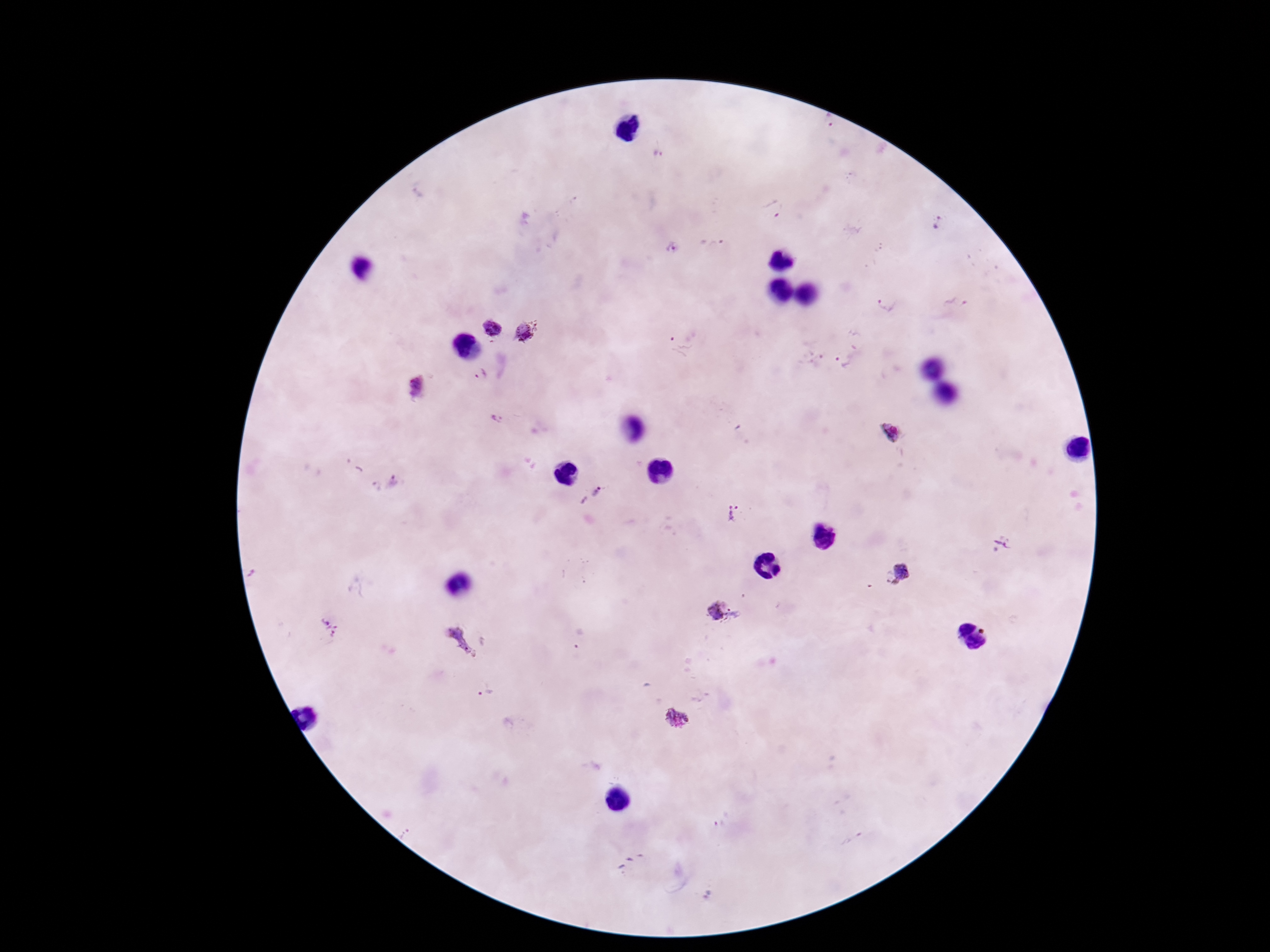
stain = Giemsa
patient malaria status = positive
preparation = thick blood smear
Plasmodium parasite locations = approximate centers as [x, y] in pixels: [828, 122], [656, 154], [775, 209], [937, 223], [674, 248], [954, 297], [888, 304], [492, 327], [526, 332], [677, 348], [843, 364], [479, 374], [415, 390], [496, 420], [889, 433], [395, 483], [374, 486], [592, 495], [732, 513], [1000, 544], [895, 575], [723, 614], [331, 631], [461, 641], [485, 692], [677, 718]
field of view = single
image size = 1270×952 pixels
capture = smartphone camera through the microscope eyepiece
magnification = 100x